Mark where leukocytes are.
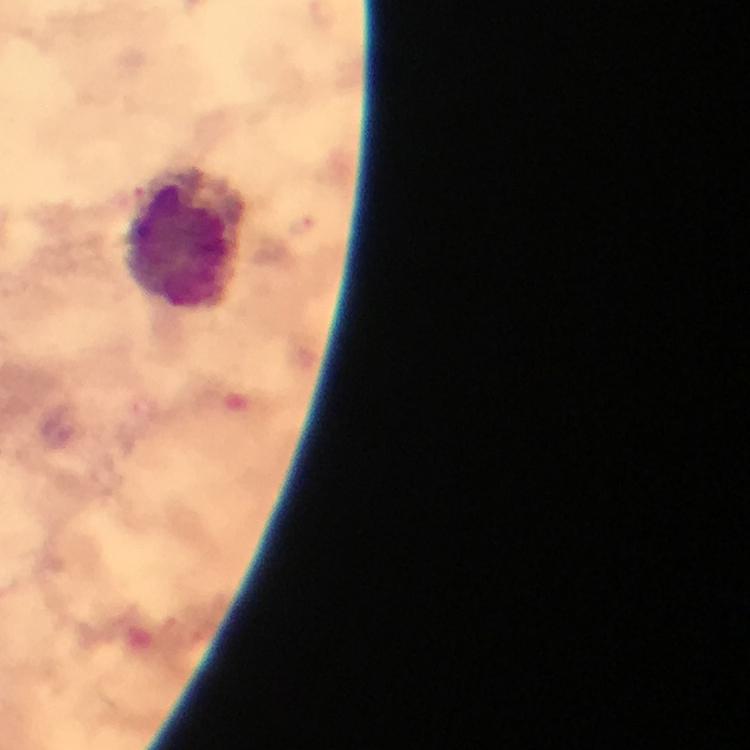
Approximate centers as {x, y} in pixels.
Leukocytes: {186, 240}.

Cropped region of a single field of view. Smartphone photograph taken through a microscope. From a diagnostic examination for malaria. Immersion oil applied. Thick blood film. Plasmodium parasites: none detected. Giemsa-stained preparation. Image is 750×750 pixels. 100x magnification.